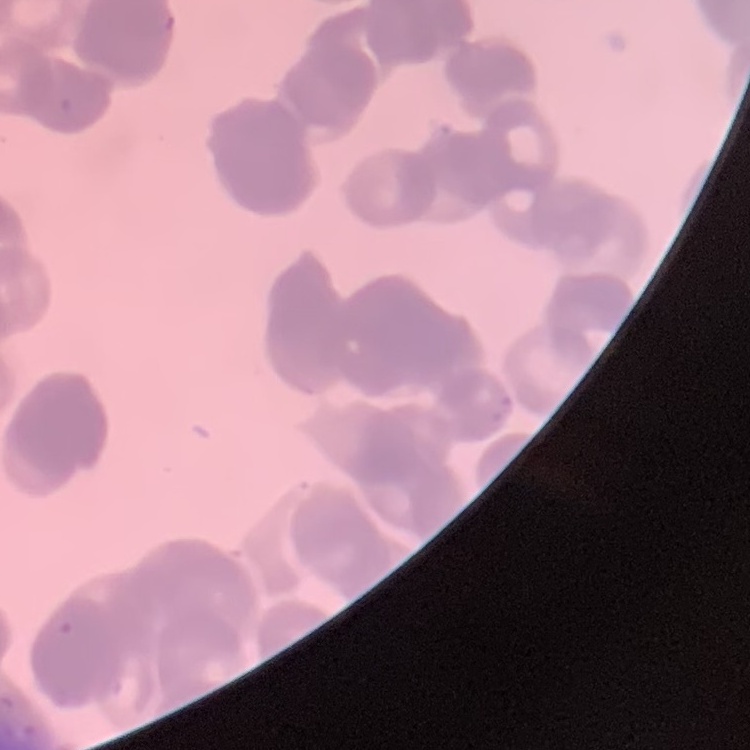

erythrocyte morphology = rouleaux formation
preparation = thin blood smear
stain = Field's or Giemsa
image type = one tile cut from a larger photomicrograph